Outline each blood parasite and name the species.
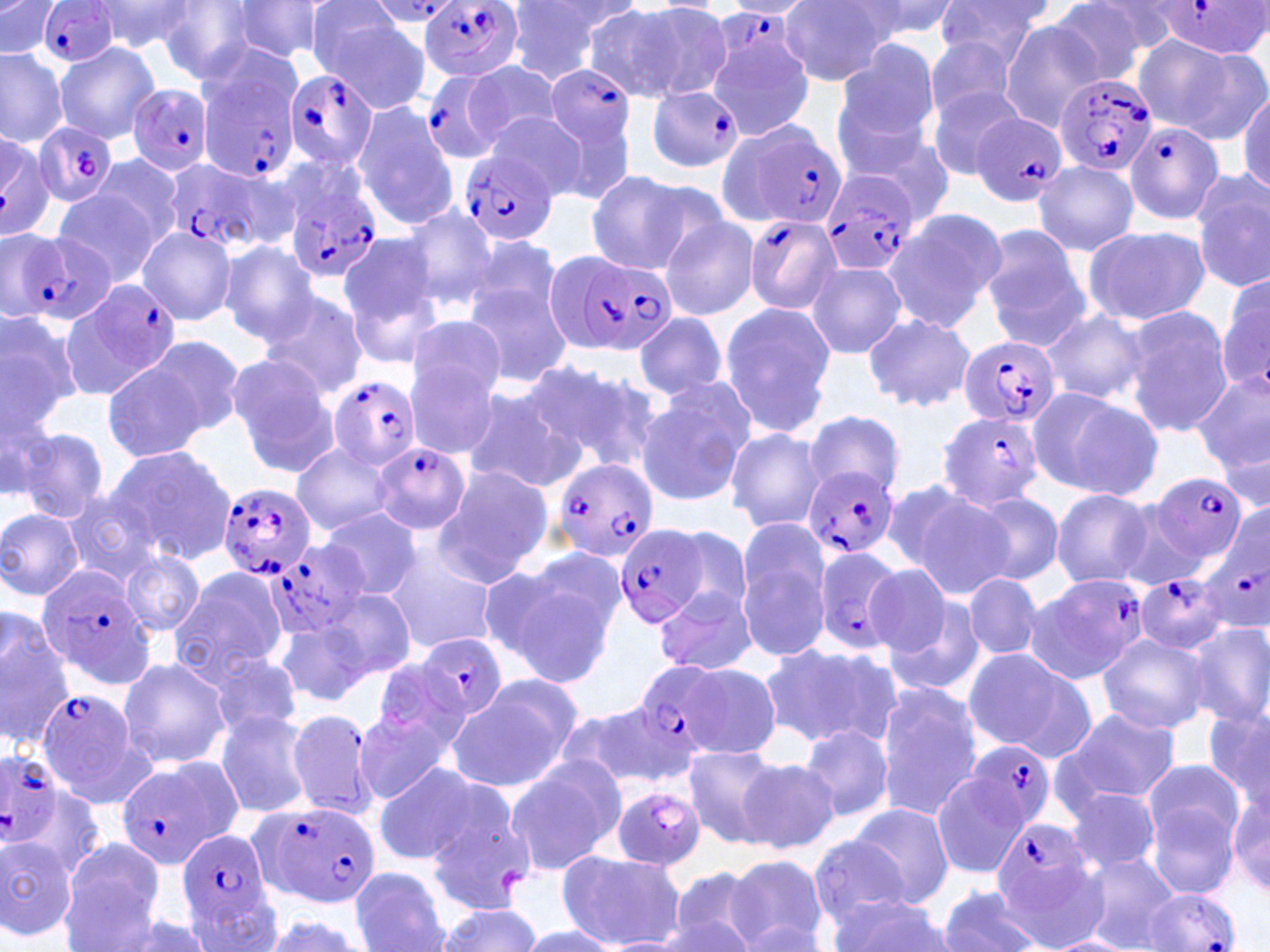
Approximate bounding boxes as named x1/y1/x2/y2 corners in pixels.
Plasmodium falciparum-infected red blood cells (subset): (x1=1154, y1=0, x2=1270, y2=60), (x1=366, y1=2, x2=461, y2=26), (x1=37, y1=3, x2=120, y2=68), (x1=419, y1=3, x2=526, y2=82), (x1=713, y1=8, x2=791, y2=71), (x1=196, y1=57, x2=299, y2=181), (x1=539, y1=63, x2=638, y2=168), (x1=283, y1=69, x2=379, y2=172), (x1=418, y1=70, x2=508, y2=164), (x1=1052, y1=71, x2=1156, y2=177), (x1=127, y1=84, x2=214, y2=176), (x1=646, y1=86, x2=744, y2=174), (x1=972, y1=113, x2=1070, y2=206), (x1=720, y1=117, x2=845, y2=232), (x1=1122, y1=121, x2=1224, y2=225), (x1=32, y1=122, x2=120, y2=207), (x1=0, y1=131, x2=54, y2=239), (x1=459, y1=149, x2=557, y2=246), (x1=163, y1=160, x2=264, y2=257), (x1=818, y1=167, x2=920, y2=276), (x1=282, y1=168, x2=382, y2=283), (x1=742, y1=215, x2=841, y2=314), (x1=20, y1=228, x2=113, y2=323), (x1=550, y1=250, x2=675, y2=358), (x1=67, y1=278, x2=183, y2=393), (x1=957, y1=336, x2=1061, y2=426), (x1=328, y1=376, x2=418, y2=471), (x1=937, y1=410, x2=1045, y2=510), (x1=375, y1=443, x2=469, y2=534), (x1=554, y1=459, x2=660, y2=564), (x1=803, y1=464, x2=897, y2=561), (x1=1150, y1=472, x2=1247, y2=569), (x1=217, y1=482, x2=319, y2=581), (x1=1199, y1=510, x2=1270, y2=638), (x1=615, y1=524, x2=711, y2=629), (x1=270, y1=538, x2=371, y2=638), (x1=811, y1=544, x2=904, y2=657), (x1=1134, y1=571, x2=1228, y2=655), (x1=1030, y1=573, x2=1150, y2=684), (x1=416, y1=632, x2=508, y2=723), (x1=35, y1=687, x2=151, y2=808), (x1=965, y1=740, x2=1057, y2=837), (x1=0, y1=750, x2=67, y2=850), (x1=611, y1=785, x2=708, y2=872), (x1=250, y1=800, x2=381, y2=908), (x1=992, y1=820, x2=1093, y2=922), (x1=178, y1=827, x2=277, y2=935), (x1=1145, y1=887, x2=1243, y2=952).
No Plasmodium ovale, Plasmodium malariae, Plasmodium vivax, Babesia divergens, or Trypanosoma brucei observed.

Uninfected red blood cell locations (subset): (x1=503, y1=0, x2=630, y2=83), (x1=844, y1=0, x2=962, y2=43), (x1=932, y1=0, x2=1050, y2=69), (x1=1045, y1=0, x2=1162, y2=86), (x1=223, y1=1, x2=329, y2=65), (x1=0, y1=2, x2=59, y2=57), (x1=86, y1=2, x2=200, y2=55), (x1=157, y1=2, x2=271, y2=83), (x1=627, y1=3, x2=733, y2=100), (x1=776, y1=3, x2=898, y2=85), (x1=582, y1=6, x2=693, y2=105), (x1=313, y1=10, x2=431, y2=111), (x1=999, y1=20, x2=1108, y2=130), (x1=1132, y1=34, x2=1262, y2=141), (x1=924, y1=35, x2=1022, y2=122), (x1=54, y1=42, x2=161, y2=143), (x1=0, y1=46, x2=69, y2=147), (x1=703, y1=48, x2=815, y2=142), (x1=840, y1=48, x2=945, y2=174), (x1=461, y1=61, x2=566, y2=148), (x1=925, y1=85, x2=1024, y2=181), (x1=1236, y1=88, x2=1269, y2=197), (x1=351, y1=103, x2=458, y2=231), (x1=537, y1=112, x2=637, y2=203), (x1=485, y1=113, x2=585, y2=200), (x1=842, y1=130, x2=953, y2=228), (x1=86, y1=153, x2=189, y2=255), (x1=1031, y1=159, x2=1141, y2=256), (x1=582, y1=171, x2=698, y2=271), (x1=1188, y1=172, x2=1269, y2=292), (x1=56, y1=184, x2=168, y2=287), (x1=399, y1=204, x2=501, y2=310), (x1=884, y1=207, x2=1008, y2=334), (x1=658, y1=216, x2=760, y2=321), (x1=1081, y1=224, x2=1211, y2=328), (x1=136, y1=225, x2=236, y2=326), (x1=979, y1=228, x2=1090, y2=349), (x1=337, y1=232, x2=444, y2=358), (x1=463, y1=234, x2=565, y2=329), (x1=218, y1=241, x2=321, y2=345), (x1=806, y1=260, x2=907, y2=359), (x1=1215, y1=265, x2=1268, y2=399), (x1=463, y1=279, x2=573, y2=388), (x1=257, y1=289, x2=367, y2=400), (x1=718, y1=302, x2=834, y2=439), (x1=1122, y1=305, x2=1235, y2=437), (x1=0, y1=307, x2=82, y2=431), (x1=1040, y1=308, x2=1152, y2=407), (x1=864, y1=311, x2=975, y2=413), (x1=632, y1=313, x2=729, y2=399), (x1=405, y1=314, x2=508, y2=401), (x1=141, y1=334, x2=249, y2=439), (x1=227, y1=353, x2=340, y2=476), (x1=101, y1=358, x2=208, y2=463), (x1=521, y1=359, x2=650, y2=467), (x1=405, y1=363, x2=500, y2=459), (x1=1195, y1=369, x2=1270, y2=478), (x1=461, y1=384, x2=583, y2=495), (x1=0, y1=386, x2=56, y2=503), (x1=1027, y1=386, x2=1160, y2=500), (x1=634, y1=388, x2=750, y2=509), (x1=803, y1=410, x2=906, y2=499), (x1=14, y1=426, x2=111, y2=521), (x1=724, y1=427, x2=828, y2=533), (x1=291, y1=441, x2=396, y2=535), (x1=106, y1=445, x2=237, y2=563), (x1=431, y1=466, x2=551, y2=588), (x1=888, y1=484, x2=1009, y2=599), (x1=1051, y1=489, x2=1153, y2=588), (x1=963, y1=490, x2=1064, y2=587), (x1=1111, y1=490, x2=1219, y2=591), (x1=61, y1=496, x2=165, y2=587), (x1=0, y1=507, x2=85, y2=602), (x1=318, y1=508, x2=419, y2=600), (x1=735, y1=522, x2=832, y2=660), (x1=668, y1=527, x2=752, y2=619), (x1=380, y1=544, x2=498, y2=653), (x1=120, y1=550, x2=206, y2=638), (x1=495, y1=561, x2=619, y2=684), (x1=861, y1=564, x2=957, y2=657), (x1=169, y1=567, x2=290, y2=680), (x1=963, y1=573, x2=1042, y2=661), (x1=656, y1=584, x2=759, y2=678), (x1=316, y1=589, x2=416, y2=684), (x1=883, y1=592, x2=986, y2=698), (x1=0, y1=610, x2=73, y2=747), (x1=274, y1=617, x2=377, y2=706), (x1=1182, y1=620, x2=1270, y2=729), (x1=1097, y1=633, x2=1210, y2=734), (x1=763, y1=643, x2=900, y2=748), (x1=196, y1=645, x2=305, y2=740), (x1=960, y1=648, x2=1092, y2=761), (x1=118, y1=656, x2=231, y2=771), (x1=367, y1=662, x2=472, y2=761), (x1=448, y1=674, x2=584, y2=794), (x1=874, y1=684, x2=985, y2=821), (x1=561, y1=699, x2=689, y2=790), (x1=1202, y1=703, x2=1270, y2=809), (x1=285, y1=707, x2=375, y2=819), (x1=1054, y1=707, x2=1180, y2=811), (x1=214, y1=708, x2=315, y2=818), (x1=355, y1=709, x2=455, y2=804), (x1=799, y1=723, x2=893, y2=823), (x1=680, y1=744, x2=787, y2=847), (x1=739, y1=756, x2=839, y2=853), (x1=503, y1=757, x2=625, y2=874), (x1=1139, y1=758, x2=1247, y2=872), (x1=374, y1=765, x2=480, y2=864), (x1=930, y1=770, x2=1031, y2=879), (x1=1228, y1=786, x2=1269, y2=897), (x1=1064, y1=787, x2=1162, y2=876), (x1=850, y1=805, x2=953, y2=909), (x1=808, y1=834, x2=908, y2=928), (x1=0, y1=836, x2=76, y2=939), (x1=60, y1=839, x2=167, y2=948), (x1=556, y1=850, x2=684, y2=950), (x1=1080, y1=853, x2=1182, y2=952), (x1=724, y1=855, x2=828, y2=952), (x1=350, y1=867, x2=449, y2=951), (x1=663, y1=869, x2=767, y2=952), (x1=938, y1=885, x2=1046, y2=952), (x1=184, y1=892, x2=282, y2=951), (x1=828, y1=898, x2=954, y2=951), (x1=433, y1=903, x2=544, y2=951), (x1=101, y1=911, x2=222, y2=952), (x1=259, y1=913, x2=365, y2=951), (x1=516, y1=926, x2=619, y2=950), (x1=1047, y1=935, x2=1133, y2=952). Slide-level diagnosis: Plasmodium falciparum. May-Grünwald-Giemsa-stained preparation. Single field of view. Captured at 1000x magnification. Thin blood film. Light microscopy. Image is 1270×952 pixels.